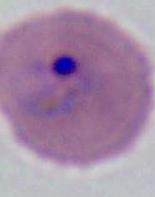

magnification = 400x or 1000x
modality = micrograph
identification = Plasmodium